State which cell type is depicted.
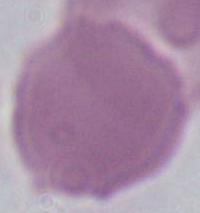

An erythrocyte.

modality = micrograph
magnification = 1000x